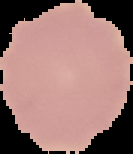
preparation = thin blood smear
image type = segmented cell region on a black background
malaria status = uninfected
image size = 133×154 pixels